Report the malaria status of this cell.
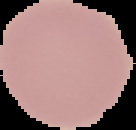
It is uninfected.

{
  "image_type": "segmented cell region with the area outside set to black",
  "image_size": "136×130 pixels",
  "preparation": "thin blood film"
}